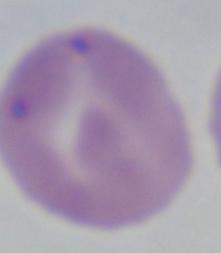

Photomicrograph. A Babesia parasite is shown. 1000x magnification.